Assess this cell for malaria.
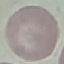

It is uninfected.

Photographed with a smartphone camera at the microscope eyepiece. Automatically extracted cell patch, resized to 64 × 64 pixels. Giemsa-stained preparation. Thin blood film.